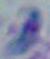
modality: photomicrograph
magnification: 1000x
identification: Toxoplasma gondii